Classify this cell by malaria status.
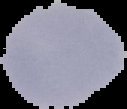
Uninfected.

Summary:
  - Preparation: thin blood film
  - Image size: 127×109 pixels
  - Image type: segmented cell region on a black background